Locate platelets.
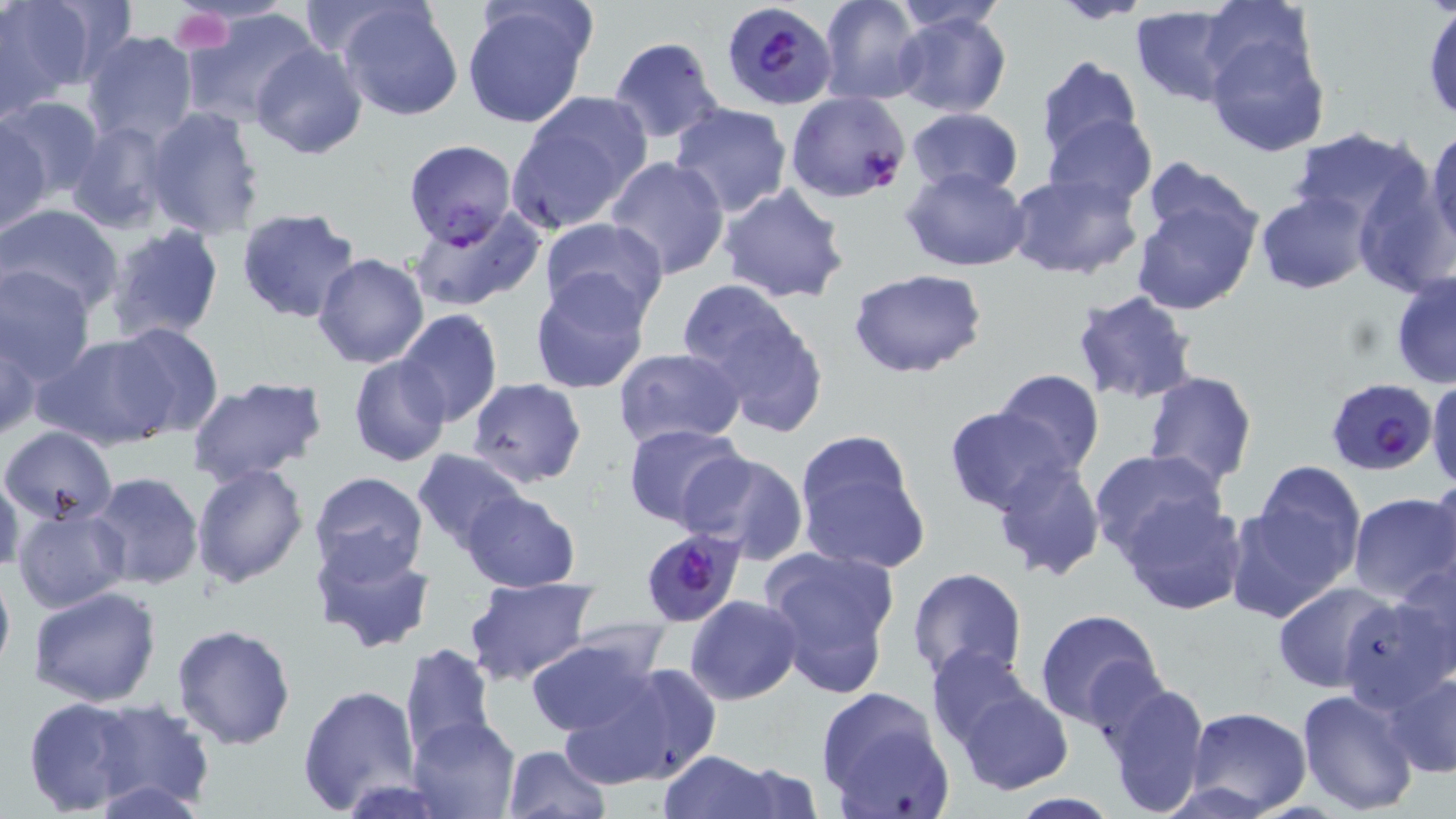

Approximate bounding boxes as (x1, y1, x2, y2) in pixels.
Platelets: (170, 6, 235, 54).

slide-level diagnosis = Plasmodium falciparum
stain = May-Grünwald-Giemsa
magnification = 1000x
modality = optical microscopy
image size = 1456×819 pixels
preparation = thin blood film
Plasmodium falciparum-infected red blood cell locations = approximate bounding boxes as (x1, y1, x2, y2) in pixels: (721, 2, 836, 111), (785, 91, 910, 204), (403, 139, 517, 246), (1325, 377, 1437, 476), (636, 526, 747, 630)
field of view = one of a larger specimen
uninfected red blood cell locations = approximate bounding boxes as (x1, y1, x2, y2) in pixels: (820, 0, 927, 104), (1056, 0, 1147, 25), (891, 1, 1007, 34), (1196, 1, 1320, 99), (0, 2, 91, 113), (293, 2, 415, 60), (336, 2, 465, 122), (460, 2, 595, 129), (1423, 3, 1456, 123), (1129, 7, 1245, 107), (182, 8, 319, 127), (893, 10, 1013, 119), (83, 30, 199, 147), (1203, 31, 1330, 157), (608, 36, 725, 143), (250, 44, 368, 159), (1033, 55, 1144, 162), (507, 95, 649, 231), (0, 97, 103, 199), (668, 103, 793, 218), (143, 106, 266, 241), (905, 107, 1022, 197), (1044, 113, 1157, 215), (1, 120, 50, 234), (66, 120, 175, 233), (1288, 128, 1430, 233), (1426, 128, 1456, 254), (606, 156, 730, 279), (1127, 165, 1267, 318), (902, 166, 1031, 271), (1352, 169, 1456, 299), (1004, 172, 1143, 280), (718, 182, 850, 305), (1254, 190, 1373, 295), (0, 202, 125, 316), (408, 207, 546, 312), (237, 208, 364, 326), (538, 216, 668, 323), (104, 225, 224, 344), (313, 253, 429, 369), (0, 267, 95, 383), (846, 268, 991, 380), (1389, 272, 1456, 390), (530, 273, 651, 395), (677, 280, 830, 435), (1070, 288, 1199, 405), (395, 309, 502, 426), (105, 322, 224, 439), (0, 324, 40, 442), (34, 334, 175, 451), (612, 347, 745, 449), (349, 356, 452, 468), (991, 368, 1105, 474), (1142, 370, 1258, 488), (185, 377, 329, 490), (468, 378, 586, 488), (1427, 379, 1456, 492), (944, 407, 1075, 513), (622, 422, 747, 530), (2, 425, 119, 525), (793, 433, 927, 574), (1087, 448, 1228, 562), (413, 449, 528, 553), (681, 452, 809, 564), (991, 456, 1105, 582), (191, 462, 307, 588), (1247, 462, 1366, 584), (0, 468, 26, 575), (88, 470, 205, 592), (308, 471, 430, 585), (1430, 473, 1456, 594), (460, 491, 582, 591), (1347, 493, 1456, 605), (1119, 494, 1247, 615), (1224, 502, 1351, 625), (12, 506, 131, 615), (310, 537, 437, 657), (759, 544, 900, 700), (1394, 553, 1456, 681), (0, 558, 15, 681), (905, 567, 1028, 683), (463, 575, 599, 683), (1272, 582, 1399, 693), (28, 586, 162, 708), (684, 595, 801, 705), (1338, 595, 1453, 713), (1033, 609, 1164, 729), (172, 623, 295, 750), (522, 634, 664, 736), (400, 643, 497, 761), (926, 645, 1038, 748), (575, 658, 722, 785), (1386, 672, 1456, 777), (1095, 678, 1213, 816), (955, 683, 1075, 794), (297, 684, 420, 816), (815, 687, 952, 818), (1297, 688, 1419, 813), (21, 694, 164, 817), (79, 698, 215, 814), (1187, 706, 1312, 815), (408, 716, 522, 819), (501, 744, 611, 819), (659, 750, 777, 819), (724, 762, 825, 819), (1005, 793, 1124, 819)